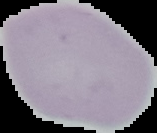

Summary:
  - Image type: segmented cell region with the area outside set to black
  - Preparation: thin blood smear
  - Image size: 157×133 pixels
  - Result: no malaria parasites seen